Report the malaria status of this cell.
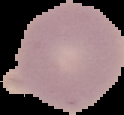
Uninfected.

From a thin blood film. Segmented cell region on a black background. Image is 124×115 pixels.